Locate every blood parasite and identify its species.
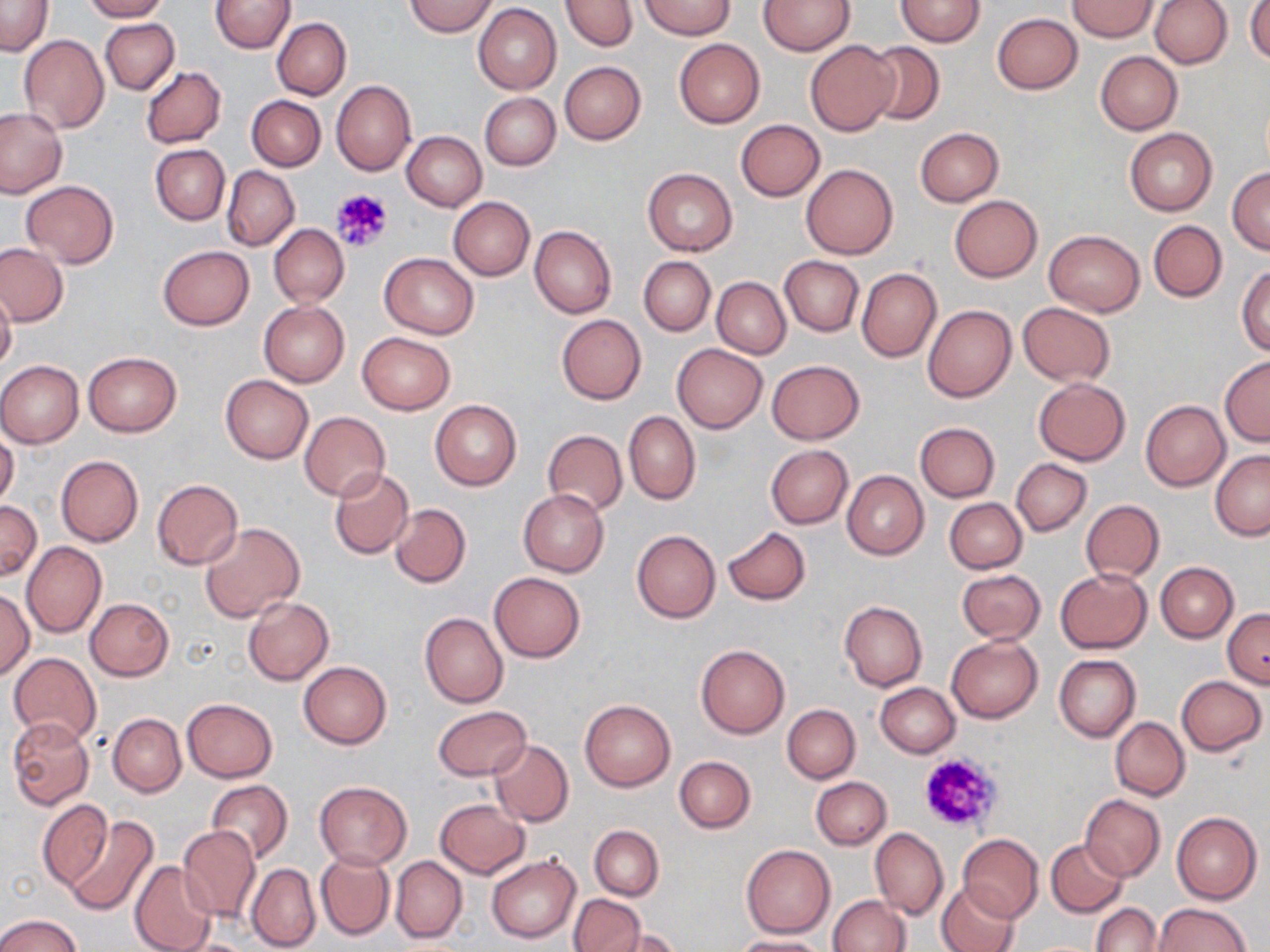

No blood parasites seen.

Approximate bounding boxes as named x1/y1/x2/y2 corners in pixels. Platelet locations: (x1=330, y1=187, x2=393, y2=254), (x1=918, y1=750, x2=1006, y2=833). Uninfected red blood cell locations: (x1=82, y1=0, x2=167, y2=21), (x1=211, y1=0, x2=293, y2=54), (x1=405, y1=0, x2=498, y2=37), (x1=639, y1=0, x2=736, y2=39), (x1=760, y1=0, x2=855, y2=55), (x1=895, y1=0, x2=986, y2=46), (x1=1150, y1=0, x2=1232, y2=69), (x1=0, y1=1, x2=53, y2=56), (x1=561, y1=1, x2=636, y2=52), (x1=1068, y1=1, x2=1159, y2=40), (x1=1246, y1=1, x2=1270, y2=65), (x1=473, y1=4, x2=561, y2=95), (x1=992, y1=12, x2=1083, y2=94), (x1=273, y1=18, x2=351, y2=99), (x1=100, y1=19, x2=179, y2=94), (x1=19, y1=34, x2=108, y2=133), (x1=674, y1=38, x2=764, y2=128), (x1=804, y1=40, x2=901, y2=136), (x1=862, y1=42, x2=944, y2=126), (x1=1096, y1=51, x2=1182, y2=134), (x1=560, y1=61, x2=646, y2=145), (x1=141, y1=66, x2=226, y2=148), (x1=331, y1=80, x2=416, y2=177), (x1=479, y1=93, x2=560, y2=171), (x1=247, y1=95, x2=326, y2=171), (x1=0, y1=108, x2=66, y2=197), (x1=736, y1=119, x2=825, y2=199), (x1=914, y1=127, x2=1004, y2=206), (x1=1125, y1=128, x2=1218, y2=216), (x1=403, y1=131, x2=487, y2=211), (x1=150, y1=145, x2=229, y2=224), (x1=802, y1=164, x2=898, y2=259), (x1=223, y1=166, x2=299, y2=250), (x1=642, y1=167, x2=738, y2=256), (x1=1227, y1=167, x2=1270, y2=254), (x1=21, y1=181, x2=119, y2=268), (x1=949, y1=195, x2=1043, y2=282), (x1=449, y1=196, x2=535, y2=280), (x1=1148, y1=220, x2=1226, y2=302), (x1=268, y1=224, x2=349, y2=306), (x1=529, y1=226, x2=616, y2=318), (x1=1043, y1=229, x2=1144, y2=317), (x1=0, y1=243, x2=69, y2=327), (x1=158, y1=245, x2=253, y2=329), (x1=379, y1=253, x2=480, y2=338), (x1=639, y1=256, x2=715, y2=336), (x1=780, y1=256, x2=863, y2=335), (x1=780, y1=264, x2=937, y2=347), (x1=1236, y1=264, x2=1270, y2=355), (x1=856, y1=269, x2=941, y2=361), (x1=712, y1=277, x2=790, y2=357), (x1=0, y1=288, x2=16, y2=373), (x1=259, y1=301, x2=349, y2=387), (x1=1017, y1=302, x2=1116, y2=386), (x1=923, y1=304, x2=1016, y2=402), (x1=556, y1=314, x2=646, y2=404), (x1=356, y1=332, x2=456, y2=414), (x1=672, y1=343, x2=767, y2=433), (x1=83, y1=352, x2=181, y2=436), (x1=1220, y1=356, x2=1270, y2=446), (x1=767, y1=359, x2=865, y2=444), (x1=0, y1=360, x2=84, y2=447), (x1=220, y1=375, x2=313, y2=464), (x1=1034, y1=378, x2=1131, y2=466), (x1=1140, y1=400, x2=1230, y2=491), (x1=431, y1=401, x2=521, y2=489), (x1=299, y1=411, x2=391, y2=502), (x1=624, y1=412, x2=700, y2=504), (x1=915, y1=422, x2=998, y2=501), (x1=542, y1=431, x2=627, y2=515), (x1=0, y1=432, x2=19, y2=510), (x1=766, y1=445, x2=853, y2=528), (x1=1211, y1=451, x2=1270, y2=540), (x1=55, y1=455, x2=143, y2=547), (x1=1011, y1=458, x2=1092, y2=535), (x1=328, y1=467, x2=414, y2=560), (x1=842, y1=470, x2=929, y2=559), (x1=152, y1=479, x2=242, y2=569), (x1=518, y1=489, x2=609, y2=577), (x1=944, y1=498, x2=1028, y2=573), (x1=1081, y1=499, x2=1164, y2=583), (x1=0, y1=500, x2=41, y2=581), (x1=390, y1=504, x2=470, y2=588), (x1=200, y1=522, x2=305, y2=622), (x1=722, y1=527, x2=811, y2=605), (x1=631, y1=529, x2=721, y2=623), (x1=22, y1=542, x2=106, y2=638), (x1=1155, y1=561, x2=1238, y2=642), (x1=1055, y1=568, x2=1152, y2=653), (x1=957, y1=569, x2=1045, y2=642), (x1=490, y1=572, x2=584, y2=661), (x1=0, y1=589, x2=34, y2=679), (x1=243, y1=597, x2=333, y2=685), (x1=86, y1=598, x2=173, y2=680), (x1=839, y1=601, x2=927, y2=691), (x1=1223, y1=608, x2=1269, y2=687), (x1=420, y1=613, x2=508, y2=708), (x1=946, y1=635, x2=1043, y2=723), (x1=696, y1=646, x2=789, y2=738), (x1=7, y1=653, x2=101, y2=746), (x1=1054, y1=654, x2=1141, y2=741), (x1=299, y1=661, x2=392, y2=749), (x1=1177, y1=675, x2=1267, y2=755), (x1=875, y1=683, x2=960, y2=757), (x1=182, y1=697, x2=278, y2=782), (x1=579, y1=699, x2=676, y2=792), (x1=783, y1=704, x2=860, y2=783), (x1=433, y1=705, x2=531, y2=781), (x1=108, y1=714, x2=186, y2=796), (x1=7, y1=717, x2=95, y2=811), (x1=1110, y1=717, x2=1189, y2=800), (x1=489, y1=740, x2=574, y2=826), (x1=674, y1=755, x2=756, y2=832), (x1=811, y1=777, x2=891, y2=850), (x1=206, y1=780, x2=294, y2=864), (x1=315, y1=781, x2=412, y2=868), (x1=1080, y1=795, x2=1165, y2=881), (x1=37, y1=798, x2=113, y2=890), (x1=434, y1=799, x2=529, y2=877), (x1=1171, y1=811, x2=1262, y2=904), (x1=64, y1=812, x2=158, y2=915), (x1=590, y1=825, x2=663, y2=900), (x1=179, y1=826, x2=261, y2=923), (x1=870, y1=828, x2=948, y2=920), (x1=958, y1=834, x2=1043, y2=921), (x1=1045, y1=839, x2=1128, y2=916), (x1=741, y1=845, x2=836, y2=938), (x1=315, y1=850, x2=394, y2=940), (x1=487, y1=854, x2=581, y2=944), (x1=390, y1=856, x2=467, y2=943), (x1=130, y1=861, x2=218, y2=952), (x1=246, y1=864, x2=321, y2=952), (x1=935, y1=880, x2=1019, y2=952), (x1=569, y1=894, x2=645, y2=951), (x1=828, y1=895, x2=910, y2=951), (x1=1091, y1=903, x2=1160, y2=952), (x1=1153, y1=903, x2=1251, y2=952), (x1=0, y1=913, x2=84, y2=952), (x1=606, y1=929, x2=683, y2=952), (x1=733, y1=936, x2=828, y2=952), (x1=168, y1=938, x2=262, y2=952). Slide-level diagnosis: negative for blood parasites. 1000x magnification. Single field of view. Thin blood smear. May-Grünwald-Giemsa stain. Light microscopy. Image is 1270×952 pixels.